State the blood parasite species.
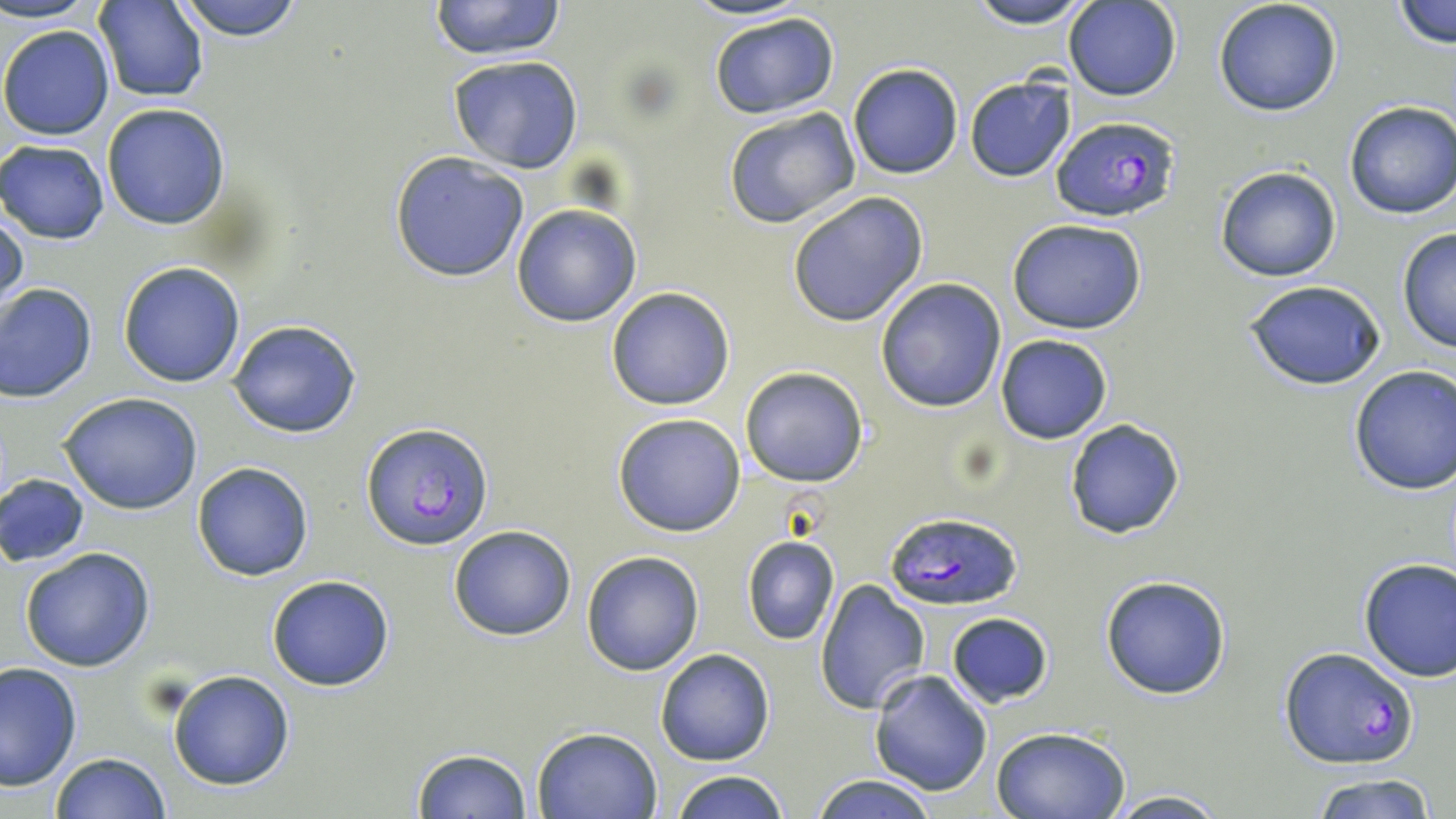
Plasmodium falciparum.

Summary:
  - Coordinate format: approximate bounding boxes as [x1, y1, x2, y2] in pixels
  - Plasmodium falciparum-infected red blood cell locations: [1050, 115, 1179, 223], [362, 422, 494, 549], [884, 510, 1023, 611], [1277, 646, 1421, 771]
  - Uninfected red blood cell locations: [2, 0, 102, 24], [170, 0, 306, 40], [426, 0, 568, 60], [678, 0, 812, 21], [962, 0, 1095, 28], [1063, 0, 1181, 101], [1212, 0, 1345, 118], [96, 1, 209, 102], [1391, 1, 1455, 49], [708, 12, 841, 119], [1, 23, 115, 140], [448, 54, 584, 173], [848, 63, 964, 179], [964, 75, 1077, 184], [1344, 99, 1456, 221], [101, 104, 230, 230], [722, 105, 860, 229], [0, 140, 109, 243], [387, 152, 532, 282], [1214, 164, 1342, 283], [784, 191, 929, 326], [1, 203, 28, 313], [511, 203, 642, 327], [1007, 219, 1149, 334], [1396, 228, 1456, 352], [118, 261, 247, 386], [875, 278, 1007, 413], [1242, 279, 1386, 391], [0, 282, 98, 402], [605, 286, 735, 410], [227, 319, 364, 439], [993, 333, 1114, 444], [1347, 364, 1456, 496], [739, 366, 869, 487], [59, 393, 204, 514], [611, 413, 748, 536], [1063, 419, 1185, 538], [191, 461, 315, 582], [0, 473, 90, 567], [448, 525, 577, 641], [741, 536, 840, 645], [20, 547, 156, 671], [581, 551, 705, 676], [1356, 556, 1456, 681], [778, 557, 890, 698], [265, 573, 397, 692], [1100, 574, 1232, 699], [813, 579, 932, 716], [945, 613, 1054, 708], [655, 648, 775, 767], [1, 661, 82, 791], [167, 670, 295, 791], [868, 671, 994, 798], [992, 726, 1135, 819], [532, 727, 662, 817], [410, 748, 534, 819], [49, 752, 172, 818], [672, 769, 790, 819], [1308, 770, 1440, 819], [806, 773, 944, 819], [1104, 789, 1229, 819]
  - Field of view: single
  - Modality: optical microscopy
  - Preparation: thin blood smear
  - Magnification: 1000x
  - Stain: May-Grünwald-Giemsa
  - Image size: 1456×819 pixels